Assess this cell for malaria.
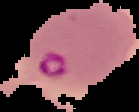

It is parasitized.

image type = segmented cell region with the area outside set to black
preparation = thin blood film
image size = 139×112 pixels